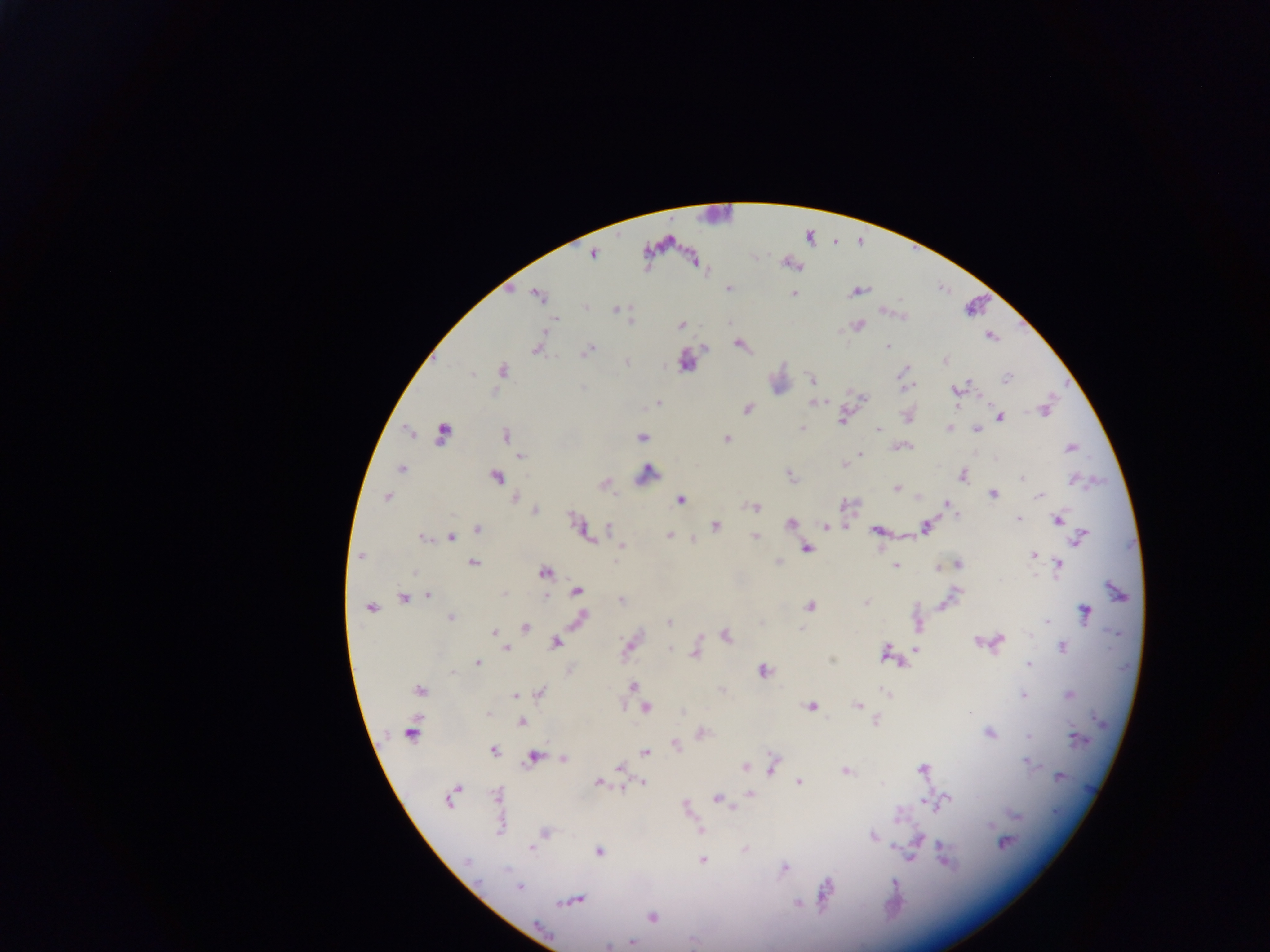

country = Ghana
field of view = single
capture = mobile-phone photograph through a microscope
malaria parasite locations = approximate centers as x y in pixels: 648 263; 647 266; 727 289; 858 292; 795 294; 536 296; 587 307; 614 310; 558 321; 631 322; 681 325; 859 325; 989 337; 738 344; 887 346; 537 348; 703 348; 587 352; 627 361; 946 362; 908 369; 501 370; 902 372; 472 376; 1006 377; 812 379; 583 388; 910 388; 955 390; 863 398; 659 401; 812 404; 748 409; 1042 410; 1029 412; 1001 417; 842 419; 801 426; 949 426; 975 430; 876 431; 441 434; 504 435; 642 437; 725 438; 906 446; 1072 448; 861 454; 520 457; 857 457; 401 470; 650 471; 963 476; 497 477; 1020 479; 897 488; 993 494; 1039 495; 918 496; 516 497; 387 498; 679 499; 947 504; 755 507; 535 510; 1019 518; 1059 518; 575 521; 790 523; 928 524; 825 526; 608 527; 477 528; 715 528; 875 530; 451 535; 588 535; 755 535; 423 536; 669 536; 1083 536; 694 539; 620 545; 808 550; 1035 554; 359 555; 473 562; 779 562; 957 563; 1059 563; 896 566; 938 568; 545 573; 415 574; 957 590; 576 591; 504 593; 427 595; 404 597; 543 599; 866 602; 811 607; 371 610; 1086 610; 581 617; 451 618; 1045 621; 669 623; 920 627; 528 628; 801 630; 495 631; 727 635; 1000 640; 977 642; 556 643; 1062 646; 629 648; 671 648; 916 648; 506 649; 885 650; 695 654; 832 660; 479 663; 900 663; 1029 663; 452 670; 764 671; 633 686; 420 691; 540 693; 885 693; 1024 694; 1069 694; 514 697; 859 705; 812 706; 645 707; 971 711; 684 712; 486 714; 521 722; 989 733; 410 734; 1027 736; 675 744; 494 751; 644 751; 534 756; 562 758; 1027 759; 1034 764; 745 766; 620 767; 923 767; 771 770; 845 771; 1058 776; 643 781; 799 782; 597 783; 624 788; 751 795; 496 798; 717 798; 450 799; 925 801; 934 802; 734 807; 990 825; 700 830; 921 835; 872 836; 1006 843; 895 844; 943 845; 532 848; 597 851; 912 858; 467 860; 946 860; 703 861; 784 868; 505 870; 519 887; 828 892; 579 899; 558 902; 566 902; 797 902; 652 918; 631 942; 606 947
preparation = thick blood smear
image size = 1270×952 pixels